State which parasite is depicted.
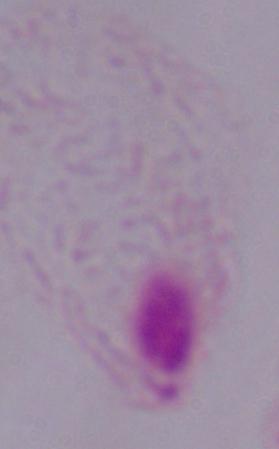

This is a trichomonad.

Summary:
  - Modality: micrograph
  - Magnification: 1000x